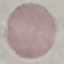
{
  "result": "no malaria parasites detected",
  "capture": "smartphone through the microscope eyepiece",
  "preparation": "thin blood film",
  "stain": "Giemsa",
  "image_type": "cell patch, automatically extracted from a larger field of view and resized to 64 × 64 pixels"
}